Classify this cell by malaria status.
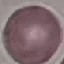
Uninfected.

Acquired by smartphone through the microscope eyepiece. Thin smear of blood. Cell patch, automatically extracted from a larger field of view and resized to 64 × 64 pixels. Giemsa-stained preparation.